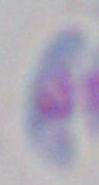

Photomicrograph. Toxoplasma gondii is shown. Captured at 1000x magnification.